Report the malaria status.
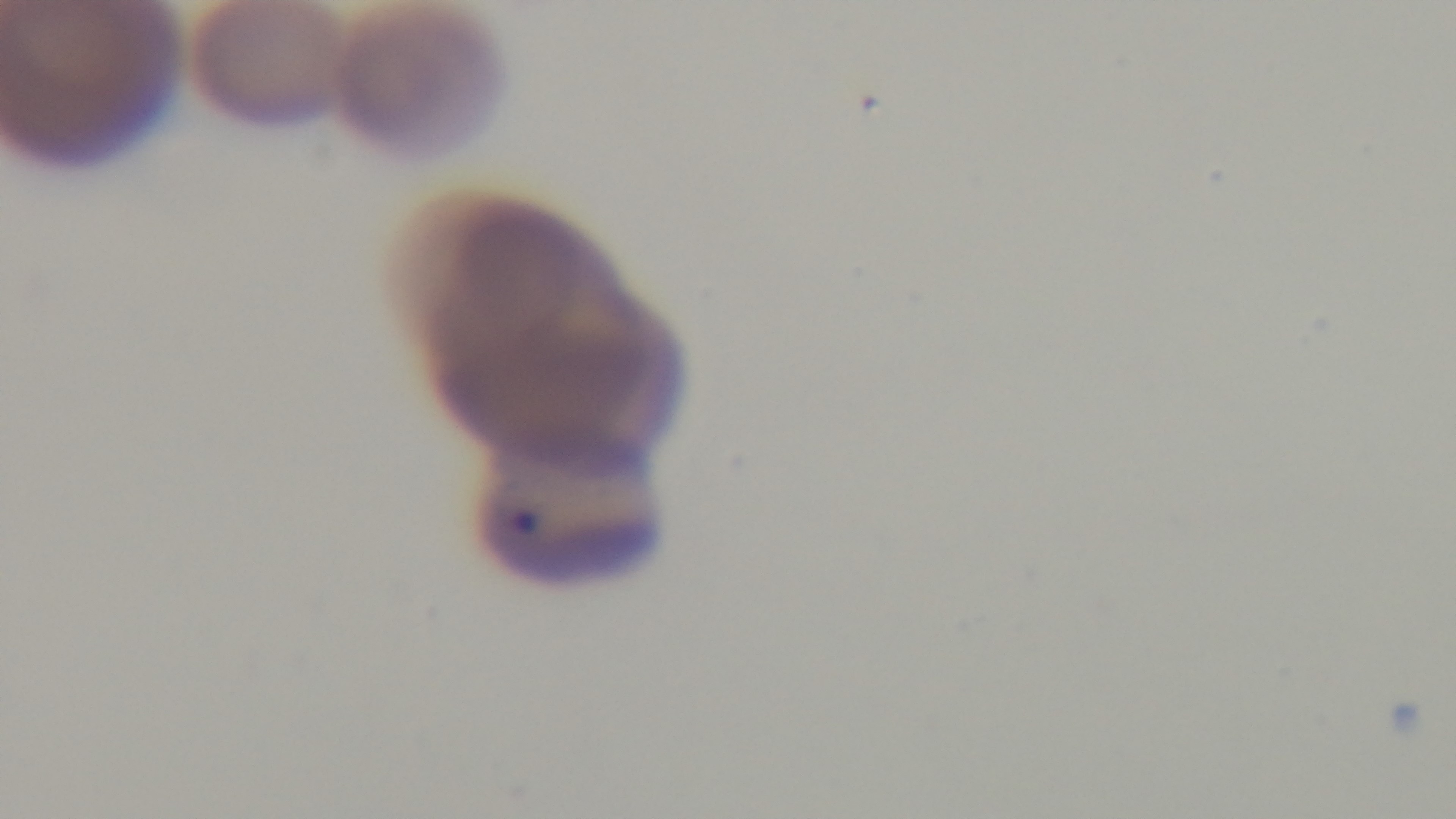

Positive.

Summary:
  - Field of view: single
  - Objective: 100x oil immersion
  - Capture: mounted 4K digital camera
  - Stain: Giemsa
  - Preparation: thin smear
  - Modality: light microscopy